Report the malaria status of this cell.
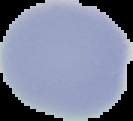
It is uninfected.

Summary:
  - Image type: cell region segmented out of the field of view; surrounding area masked to black
  - Preparation: thin blood smear
  - Image size: 133×121 pixels